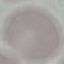

Result: no malaria parasites seen. Automatically extracted cell patch, resized to 64 × 64 pixels. Acquired by smartphone through the microscope eyepiece. Thin blood film. Giemsa-stained preparation.